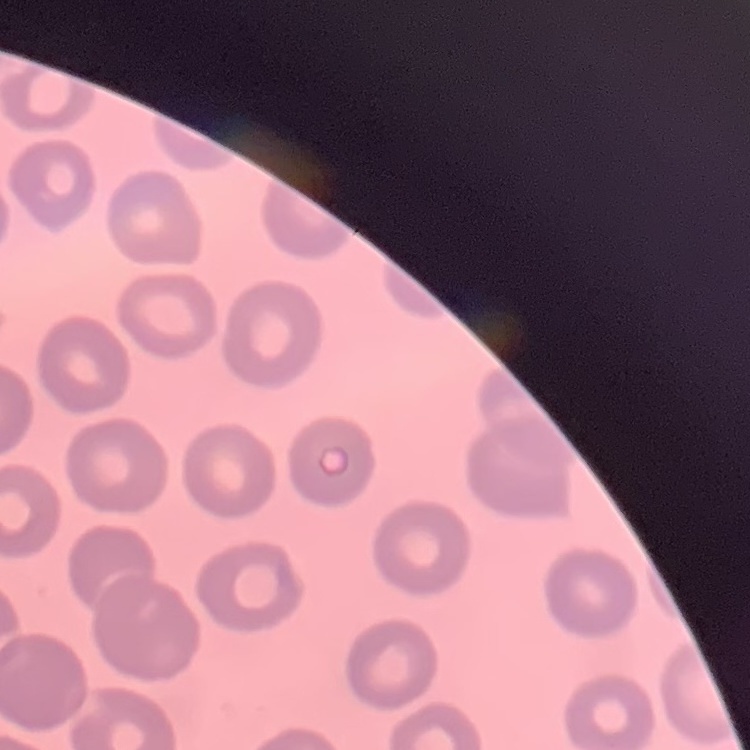
red blood cell morphology = no rouleaux formation
image type = square crop of a larger photomicrograph
stain = Field's or Giemsa
preparation = thin blood film